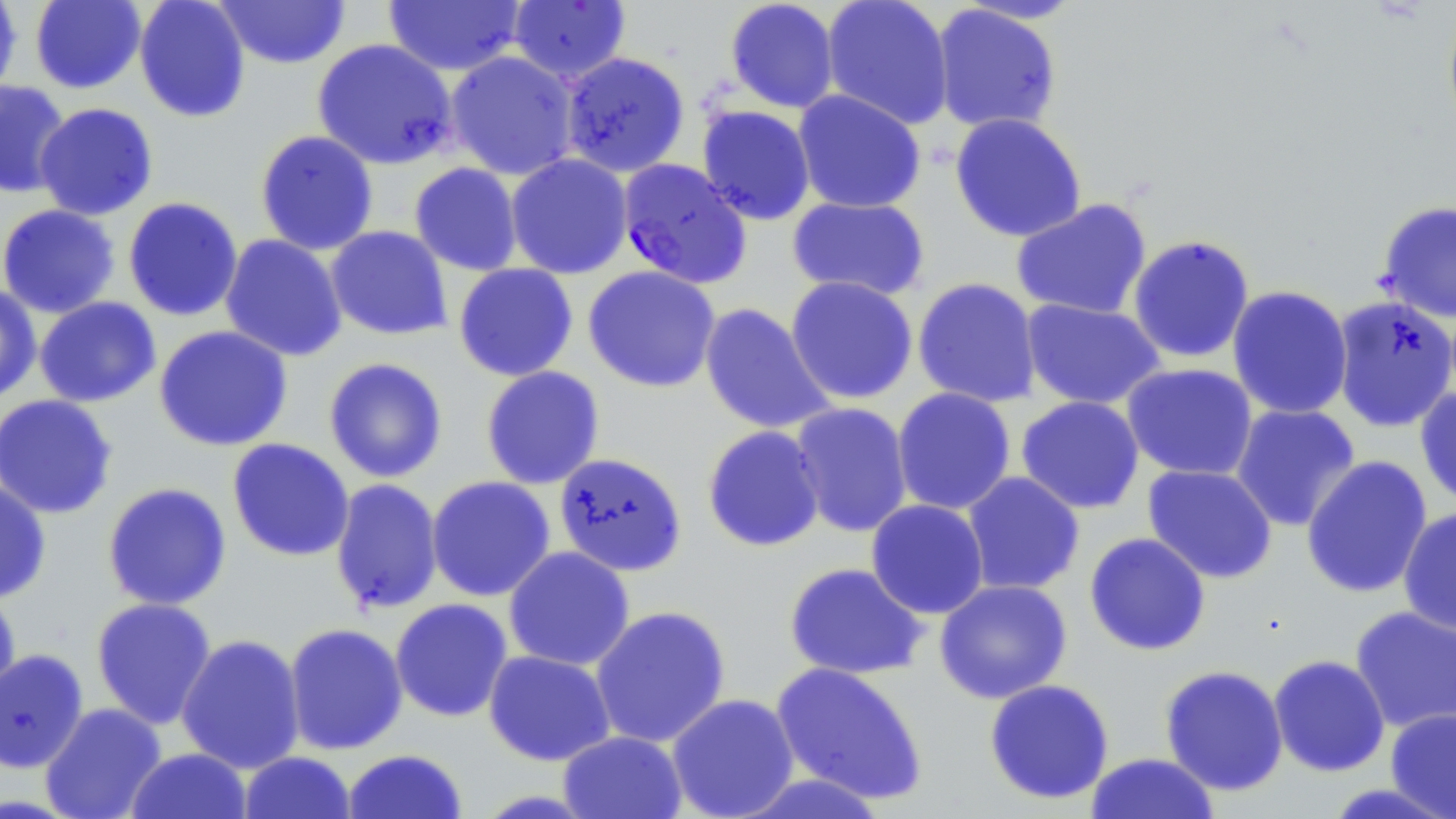 Approximate bounding boxes as named x1/y1/x2/y2 corners in pixels. Uninfected red blood cell locations: (x1=0, y1=0, x2=22, y2=100), (x1=30, y1=0, x2=146, y2=94), (x1=133, y1=0, x2=251, y2=123), (x1=213, y1=0, x2=351, y2=69), (x1=724, y1=0, x2=840, y2=113), (x1=821, y1=0, x2=954, y2=130), (x1=383, y1=1, x2=526, y2=76), (x1=507, y1=1, x2=631, y2=84), (x1=931, y1=4, x2=1062, y2=134), (x1=1442, y1=4, x2=1456, y2=138), (x1=312, y1=38, x2=458, y2=170), (x1=445, y1=51, x2=579, y2=180), (x1=561, y1=52, x2=690, y2=177), (x1=0, y1=80, x2=71, y2=199), (x1=793, y1=89, x2=926, y2=214), (x1=34, y1=102, x2=158, y2=220), (x1=697, y1=105, x2=816, y2=225), (x1=949, y1=112, x2=1087, y2=243), (x1=254, y1=130, x2=379, y2=255), (x1=506, y1=154, x2=633, y2=279), (x1=409, y1=162, x2=523, y2=276), (x1=787, y1=196, x2=930, y2=301), (x1=123, y1=197, x2=243, y2=322), (x1=1011, y1=198, x2=1152, y2=321), (x1=1376, y1=200, x2=1456, y2=323), (x1=0, y1=204, x2=120, y2=318), (x1=326, y1=226, x2=453, y2=340), (x1=220, y1=234, x2=347, y2=362), (x1=1127, y1=234, x2=1255, y2=364), (x1=453, y1=263, x2=579, y2=381), (x1=582, y1=265, x2=721, y2=393), (x1=784, y1=276, x2=919, y2=404), (x1=912, y1=277, x2=1042, y2=408), (x1=0, y1=283, x2=42, y2=405), (x1=1226, y1=285, x2=1353, y2=420), (x1=1331, y1=295, x2=1456, y2=432), (x1=34, y1=297, x2=161, y2=408), (x1=1021, y1=298, x2=1166, y2=410), (x1=699, y1=303, x2=835, y2=435), (x1=153, y1=325, x2=293, y2=451), (x1=323, y1=357, x2=449, y2=483), (x1=1121, y1=363, x2=1258, y2=480), (x1=480, y1=366, x2=605, y2=490), (x1=1414, y1=386, x2=1456, y2=510), (x1=892, y1=387, x2=1016, y2=516), (x1=0, y1=394, x2=119, y2=519), (x1=1016, y1=395, x2=1145, y2=514), (x1=789, y1=402, x2=913, y2=538), (x1=1230, y1=403, x2=1361, y2=532), (x1=701, y1=425, x2=826, y2=553), (x1=226, y1=438, x2=355, y2=562), (x1=553, y1=451, x2=688, y2=577), (x1=1301, y1=455, x2=1433, y2=599), (x1=1142, y1=464, x2=1278, y2=584), (x1=961, y1=471, x2=1085, y2=596), (x1=0, y1=475, x2=52, y2=603), (x1=426, y1=476, x2=556, y2=602), (x1=330, y1=479, x2=444, y2=615), (x1=102, y1=482, x2=232, y2=611), (x1=866, y1=499, x2=989, y2=619), (x1=1397, y1=506, x2=1456, y2=634), (x1=1084, y1=532, x2=1211, y2=656), (x1=503, y1=546, x2=635, y2=671), (x1=784, y1=562, x2=929, y2=680), (x1=934, y1=579, x2=1073, y2=704), (x1=0, y1=586, x2=21, y2=707), (x1=91, y1=597, x2=217, y2=729), (x1=390, y1=598, x2=513, y2=722), (x1=589, y1=605, x2=731, y2=748), (x1=1350, y1=606, x2=1456, y2=733), (x1=283, y1=623, x2=408, y2=755), (x1=176, y1=633, x2=306, y2=774), (x1=0, y1=649, x2=89, y2=773), (x1=483, y1=649, x2=616, y2=766), (x1=1269, y1=655, x2=1390, y2=777), (x1=770, y1=661, x2=929, y2=806), (x1=1159, y1=664, x2=1289, y2=796), (x1=983, y1=678, x2=1115, y2=805), (x1=666, y1=693, x2=800, y2=819), (x1=40, y1=702, x2=167, y2=819), (x1=1385, y1=708, x2=1456, y2=818), (x1=558, y1=730, x2=687, y2=819), (x1=125, y1=748, x2=252, y2=819), (x1=342, y1=749, x2=468, y2=819), (x1=238, y1=751, x2=357, y2=818), (x1=1085, y1=752, x2=1220, y2=818), (x1=733, y1=771, x2=892, y2=818), (x1=1320, y1=782, x2=1456, y2=819). Plasmodium falciparum-infected red blood cell locations: (x1=617, y1=158, x2=751, y2=289). Slide-level diagnosis: Plasmodium falciparum. Optical microscopy. May-Grünwald-Giemsa-stained preparation. Thin blood smear. Single field of view. Captured at 1000x magnification. Image is 1456×819 pixels.